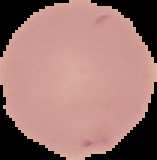

Image is 157×160 pixels. Cell region segmented out of the field of view; the surrounding area is masked to black. From a thin blood film. Result: negative for Plasmodium parasites.